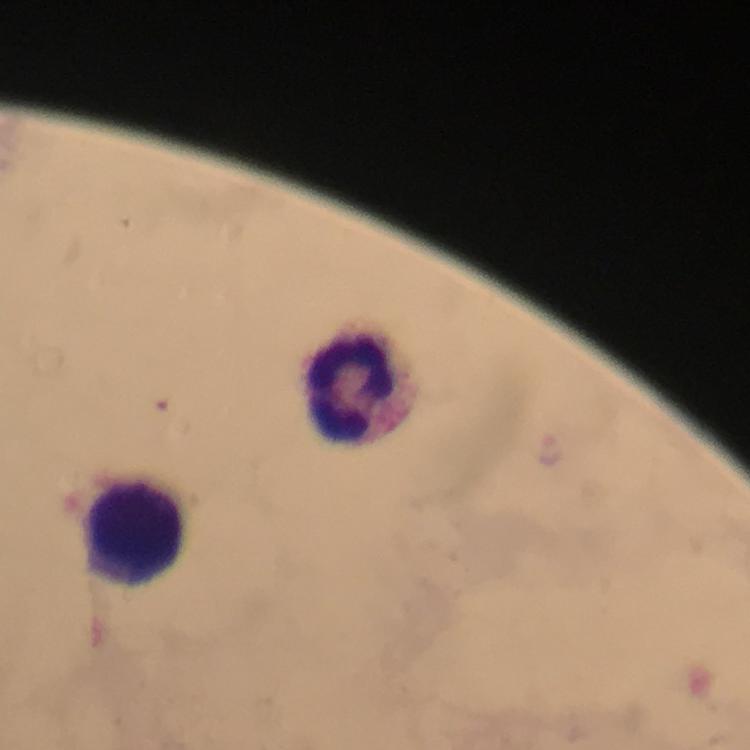
preparation: thick blood film
capture: smartphone mounted on the microscope
context: from a malaria diagnostic workup
immersion_oil: applied
image_size: 750×750 pixels
magnification: 100x
leukocyte_locations: 'approximate centers as [x, y] in pixels: [350, 385], [142, 524]'
plasmodium_parasites: none detected
cropped_from: a single field of view
stain: Giemsa